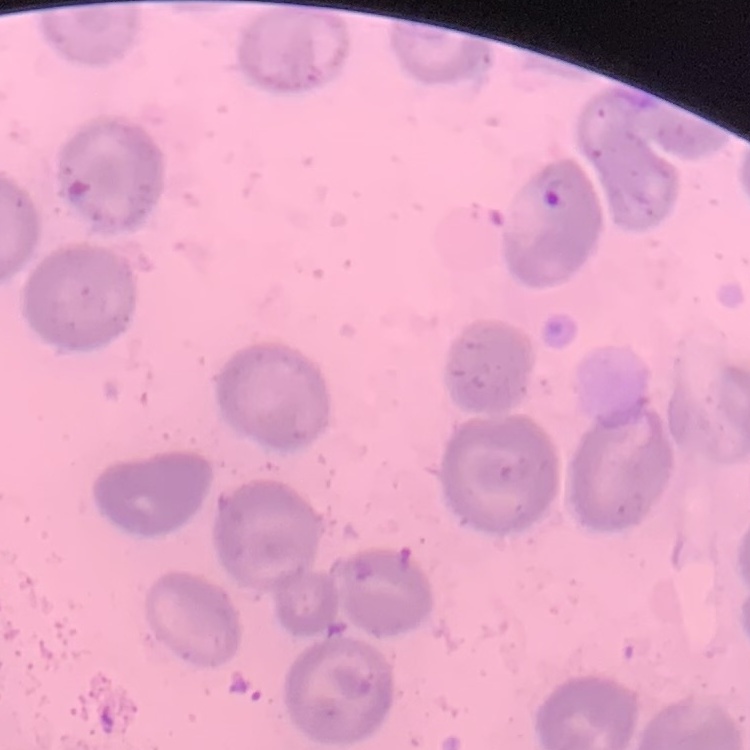
red blood cell morphology = no rouleaux formation
preparation = thin blood film
image type = one tile cut from a larger photomicrograph
stain = Field's or Giemsa